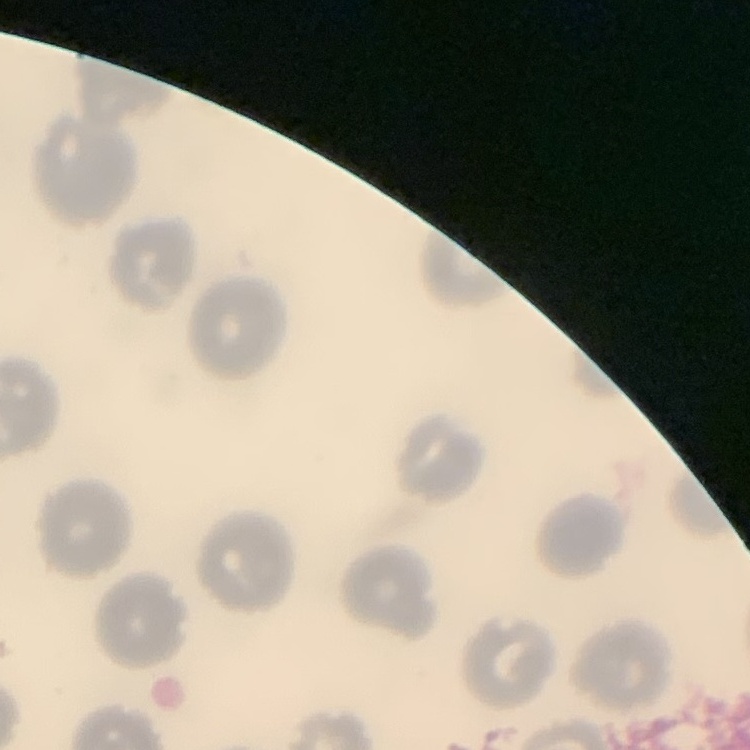
Summary:
  - Red blood cell morphology: no rouleaux formation
  - Preparation: thin peripheral smear
  - Image type: one tile cut from a larger photomicrograph
  - Stain: Field's or Giemsa